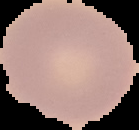

Malaria status: uninfected. Image is 139×130 pixels. Cell region segmented out of the field of view; the surrounding area is masked to black. From a thin blood smear.